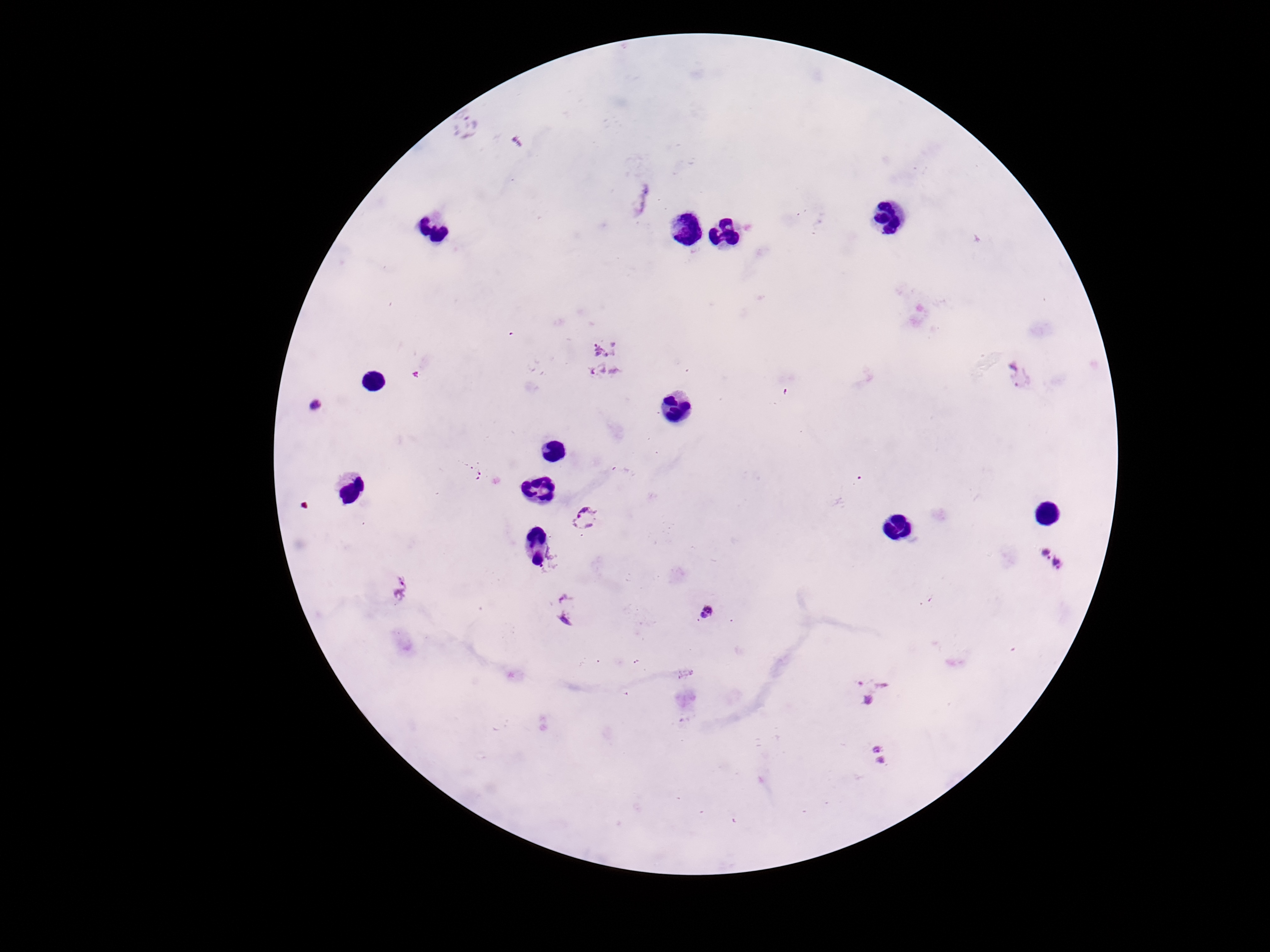
{
  "stain": "Giemsa",
  "magnification": "100x",
  "field_of_view": "one from this slide",
  "plasmodium_parasite_locations": "approximate object centers, in pixels from the top-left corner: (x=466, y=123), (x=516, y=142), (x=639, y=197), (x=601, y=343), (x=604, y=373), (x=1021, y=376), (x=314, y=405), (x=475, y=472), (x=586, y=519), (x=1042, y=550), (x=1061, y=564), (x=399, y=586), (x=564, y=607), (x=708, y=612), (x=873, y=691), (x=882, y=756)",
  "image_size": "1270×952 pixels",
  "capture": "smartphone camera through the microscope eyepiece",
  "patient_malaria_status": "positive",
  "preparation": "thick peripheral-blood smear"
}